Locate every uninfected red blood cell.
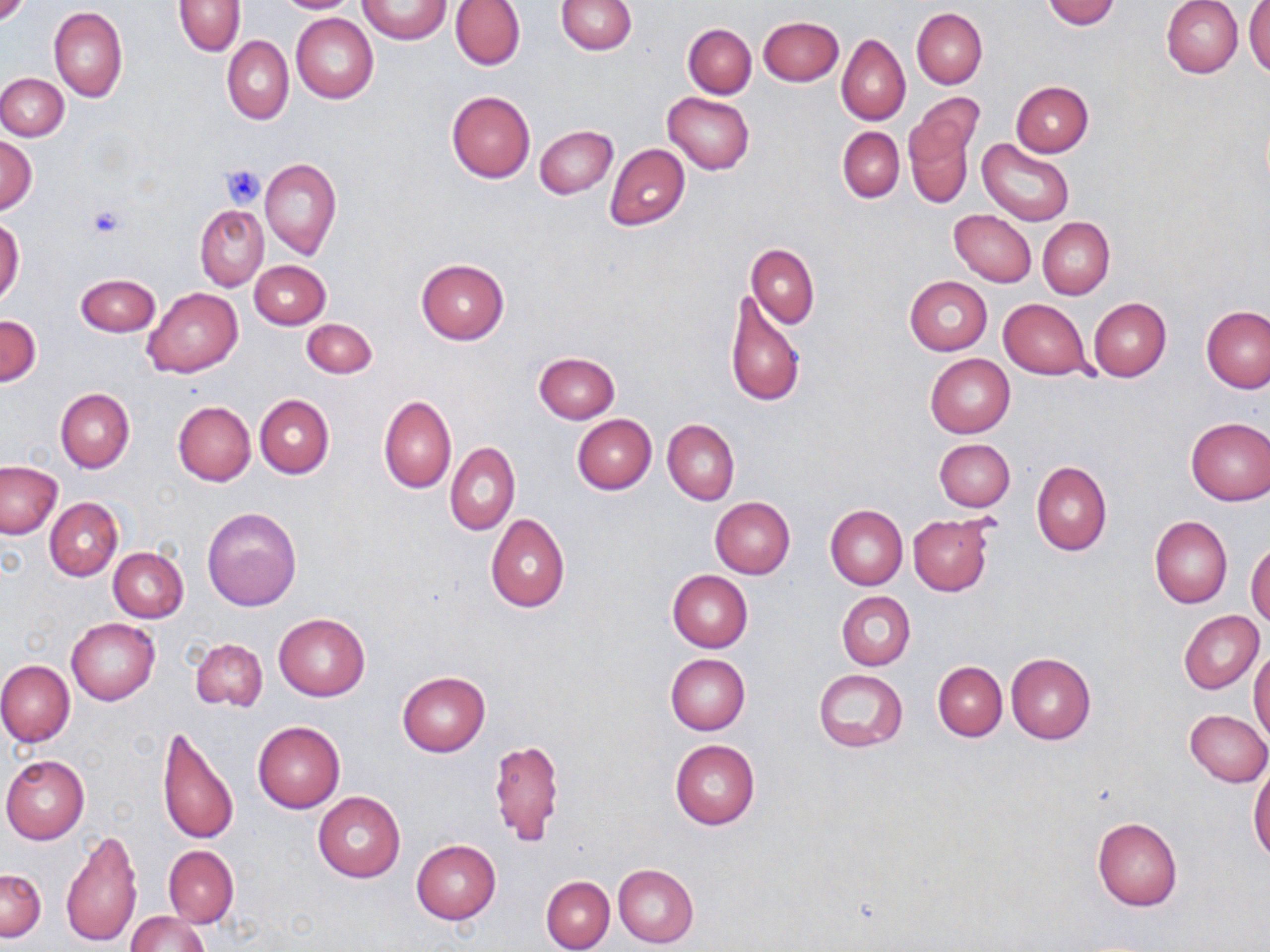

Approximate bounding boxes as named x1/y1/x2/y2 corners in pixels.
Uninfected red blood cells: (x1=273, y1=0, x2=364, y2=13), (x1=359, y1=0, x2=450, y2=44), (x1=450, y1=0, x2=524, y2=70), (x1=556, y1=0, x2=637, y2=55), (x1=1042, y1=0, x2=1121, y2=28), (x1=175, y1=1, x2=245, y2=55), (x1=1162, y1=1, x2=1243, y2=78), (x1=1246, y1=2, x2=1270, y2=80), (x1=50, y1=6, x2=127, y2=101), (x1=911, y1=8, x2=987, y2=89), (x1=292, y1=13, x2=379, y2=104), (x1=758, y1=16, x2=843, y2=85), (x1=682, y1=23, x2=756, y2=98), (x1=837, y1=35, x2=909, y2=125), (x1=223, y1=36, x2=293, y2=125), (x1=0, y1=73, x2=68, y2=140), (x1=1011, y1=81, x2=1093, y2=156), (x1=447, y1=91, x2=535, y2=183), (x1=663, y1=92, x2=755, y2=173), (x1=904, y1=101, x2=980, y2=209), (x1=535, y1=125, x2=616, y2=198), (x1=838, y1=127, x2=904, y2=202), (x1=536, y1=132, x2=687, y2=212), (x1=0, y1=136, x2=36, y2=215), (x1=977, y1=138, x2=1075, y2=225), (x1=605, y1=144, x2=690, y2=230), (x1=260, y1=158, x2=341, y2=259), (x1=195, y1=204, x2=268, y2=291), (x1=949, y1=210, x2=1037, y2=286), (x1=1038, y1=217, x2=1114, y2=299), (x1=0, y1=218, x2=23, y2=308), (x1=747, y1=242, x2=819, y2=328), (x1=416, y1=258, x2=509, y2=344), (x1=250, y1=260, x2=330, y2=328), (x1=74, y1=274, x2=160, y2=336), (x1=904, y1=275, x2=992, y2=355), (x1=143, y1=287, x2=243, y2=378), (x1=725, y1=290, x2=807, y2=409), (x1=1090, y1=298, x2=1171, y2=381), (x1=999, y1=299, x2=1091, y2=380), (x1=1202, y1=306, x2=1270, y2=393), (x1=1, y1=315, x2=42, y2=386), (x1=302, y1=318, x2=376, y2=377), (x1=533, y1=352, x2=619, y2=423), (x1=925, y1=354, x2=1015, y2=437), (x1=55, y1=389, x2=134, y2=473), (x1=255, y1=394, x2=334, y2=479), (x1=379, y1=396, x2=456, y2=494), (x1=173, y1=400, x2=255, y2=486), (x1=572, y1=415, x2=656, y2=494), (x1=1185, y1=417, x2=1269, y2=506), (x1=663, y1=419, x2=739, y2=505), (x1=933, y1=439, x2=1015, y2=510), (x1=446, y1=442, x2=519, y2=535), (x1=0, y1=461, x2=64, y2=539), (x1=1032, y1=461, x2=1112, y2=556), (x1=710, y1=497, x2=795, y2=578), (x1=45, y1=499, x2=122, y2=580), (x1=825, y1=504, x2=908, y2=589), (x1=202, y1=506, x2=302, y2=612), (x1=486, y1=514, x2=570, y2=612), (x1=909, y1=515, x2=992, y2=596), (x1=1150, y1=516, x2=1232, y2=608), (x1=1247, y1=539, x2=1270, y2=624), (x1=109, y1=547, x2=188, y2=622), (x1=668, y1=570, x2=752, y2=652), (x1=838, y1=591, x2=916, y2=670), (x1=1179, y1=610, x2=1265, y2=693), (x1=274, y1=614, x2=369, y2=701), (x1=67, y1=618, x2=160, y2=706), (x1=190, y1=638, x2=267, y2=711), (x1=1249, y1=648, x2=1270, y2=744), (x1=1006, y1=653, x2=1095, y2=743), (x1=666, y1=654, x2=750, y2=734), (x1=0, y1=660, x2=74, y2=746), (x1=933, y1=661, x2=1007, y2=740), (x1=814, y1=667, x2=908, y2=752), (x1=397, y1=670, x2=489, y2=756), (x1=1184, y1=710, x2=1270, y2=787), (x1=253, y1=721, x2=345, y2=812), (x1=155, y1=727, x2=238, y2=846), (x1=489, y1=739, x2=564, y2=846), (x1=669, y1=740, x2=760, y2=829), (x1=1, y1=754, x2=90, y2=843), (x1=1249, y1=766, x2=1270, y2=861), (x1=313, y1=793, x2=406, y2=882), (x1=1091, y1=816, x2=1183, y2=910), (x1=61, y1=828, x2=143, y2=950), (x1=411, y1=840, x2=500, y2=924), (x1=164, y1=846, x2=238, y2=927), (x1=613, y1=863, x2=698, y2=948), (x1=0, y1=867, x2=46, y2=941), (x1=541, y1=875, x2=614, y2=952), (x1=125, y1=911, x2=210, y2=952).

Summary:
  - Platelet locations: (x1=221, y1=164, x2=266, y2=207), (x1=90, y1=205, x2=125, y2=240)
  - Slide-level diagnosis: negative for blood parasites
  - Magnification: 1000x
  - Image size: 1270×952 pixels
  - Field of view: single
  - Modality: light microscopy
  - Stain: May-Grünwald-Giemsa
  - Preparation: thin blood film